Locate the cells, classifying each as a parasitized red blood cell, an uninfected red blood cell, or a white blood cell.
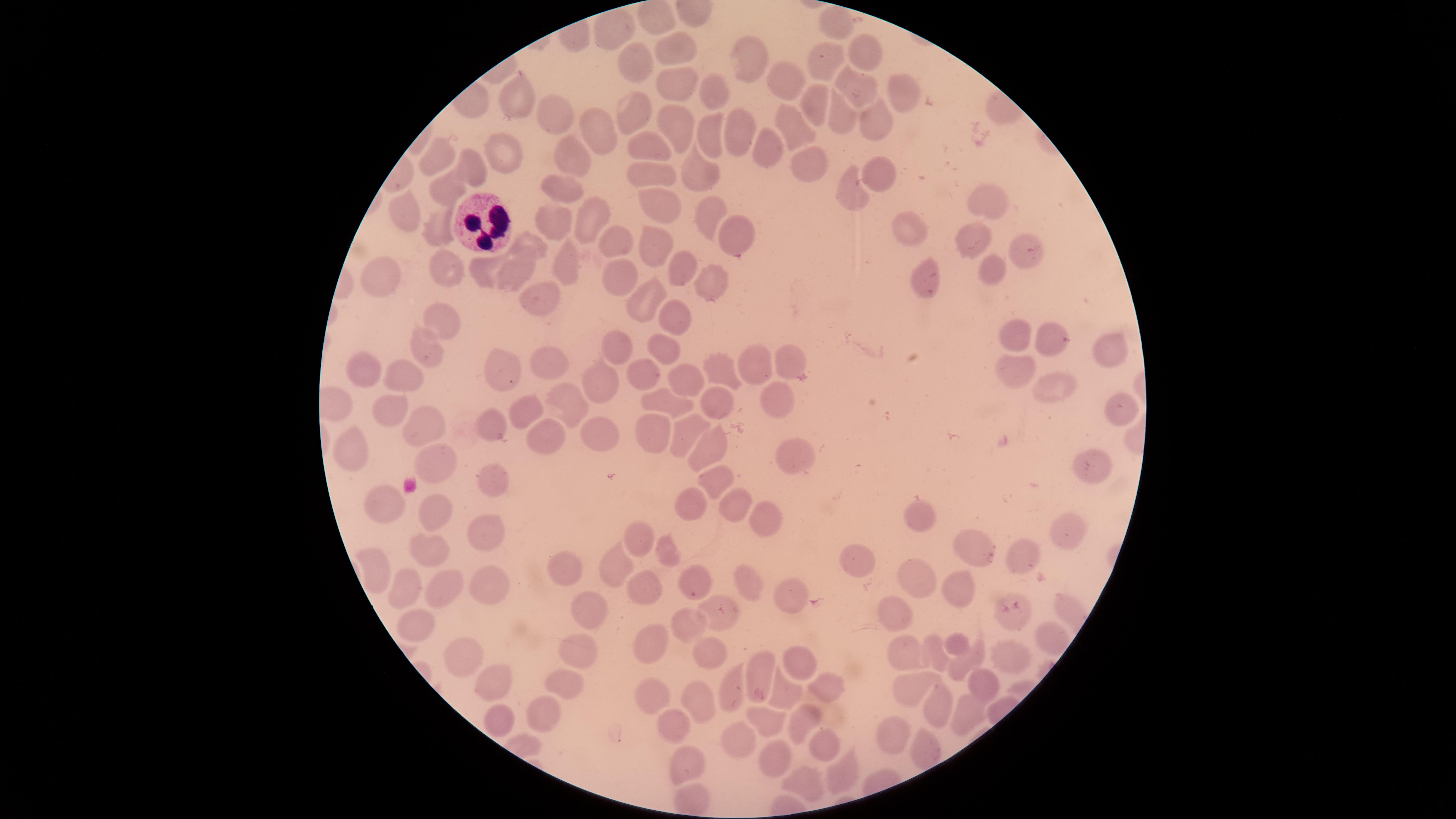

No parasitized red blood cells identified.
Approximate marker points as {x, y} in pixels.
Uninfected red blood cells: {842, 23}, {610, 32}, {681, 47}, {864, 49}, {746, 58}, {639, 63}, {828, 63}, {783, 78}, {677, 88}, {849, 89}, {710, 90}, {907, 92}, {807, 102}, {515, 103}, {554, 114}, {634, 115}, {842, 118}, {877, 124}, {677, 126}, {792, 126}, {597, 131}, {738, 131}, {712, 135}, {509, 150}, {652, 151}, {766, 151}, {441, 155}, {811, 157}, {474, 168}, {573, 168}, {876, 168}, {699, 170}, {652, 177}, {851, 187}, {446, 188}, {561, 192}, {984, 201}, {656, 205}, {411, 209}, {707, 210}, {586, 222}, {551, 225}, {439, 229}, {739, 230}, {910, 233}, {971, 237}, {616, 240}, {531, 244}, {653, 246}, {1017, 247}, {482, 263}, {445, 266}, {623, 269}, {519, 271}, {681, 271}, {997, 271}, {565, 273}, {925, 274}, {381, 279}, {708, 290}, {649, 296}, {536, 298}, {442, 318}, {674, 325}, {1017, 334}, {1047, 343}, {424, 345}, {665, 347}, {613, 348}, {1109, 353}, {793, 360}, {546, 364}, {719, 365}, {367, 367}, {758, 367}, {500, 369}, {644, 371}, {1015, 374}, {406, 377}, {595, 378}, {1057, 380}, {691, 381}, {674, 395}, {783, 397}, {1122, 399}, {574, 402}, {715, 402}, {386, 406}, {522, 412}, {493, 419}, {424, 428}, {679, 432}, {550, 435}, {603, 436}, {649, 436}, {350, 446}, {709, 448}, {796, 456}, {440, 462}, {1085, 467}, {495, 479}, {710, 481}, {385, 500}, {732, 506}, {693, 510}, {438, 514}, {767, 515}, {923, 523}, {1060, 529}, {640, 536}, {482, 538}, {431, 550}, {977, 550}, {664, 551}, {1023, 555}, {865, 561}, {381, 562}, {563, 567}, {613, 568}, {915, 580}, {690, 581}, {407, 583}, {747, 583}, {955, 587}, {646, 590}, {442, 591}, {487, 591}, {786, 594}, {593, 607}, {712, 612}, {894, 619}, {690, 622}, {413, 627}, {1049, 636}, {656, 640}, {581, 645}, {961, 645}, {916, 652}, {936, 652}, {711, 653}, {1016, 656}, {461, 658}, {977, 659}, {805, 661}, {761, 672}, {495, 681}, {563, 682}, {977, 687}, {732, 688}, {826, 688}, {651, 692}, {909, 692}, {784, 693}, {700, 703}, {937, 704}, {546, 708}, {965, 713}, {496, 723}, {800, 724}, {672, 725}, {768, 726}, {894, 736}, {737, 742}, {825, 745}, {920, 748}, {774, 758}, {685, 764}, {838, 775}, {800, 782}.
White blood cells: {480, 224}.

preparation = thin blood film
field of view = single
visible region = circular
image size = 1456×819 pixels
capture = smartphone photograph through the microscope eyepiece
stain = Giemsa